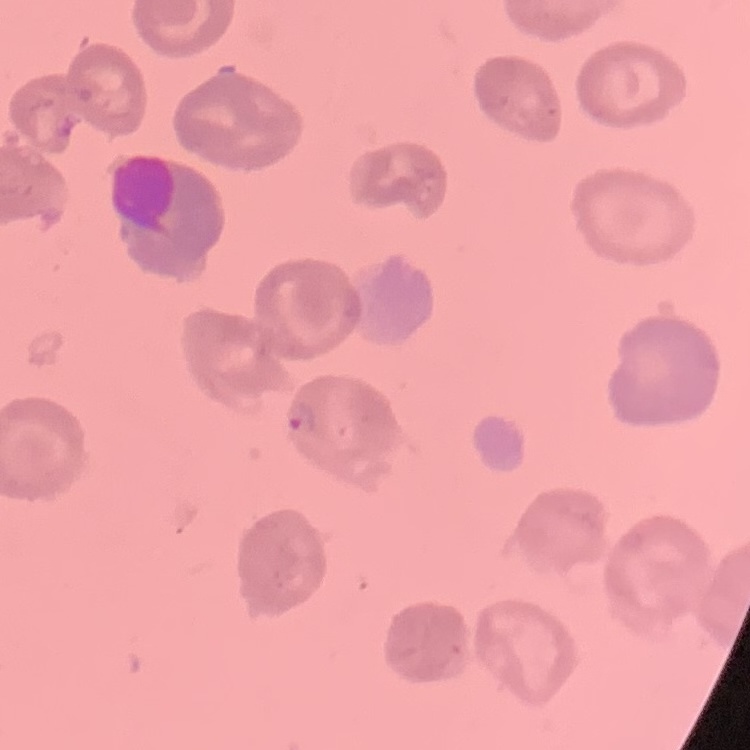

Summary:
  - Red blood cell morphology: no rouleaux formation
  - Stain: Field's or Giemsa
  - Preparation: thin peripheral smear
  - Image type: one tile cut from a larger photomicrograph